Report the malaria status of this cell.
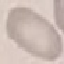
It is uninfected.

stain = Giemsa
preparation = thin blood smear
capture = smartphone through the microscope eyepiece
image type = automatically extracted cell patch, resized to 64 × 64 pixels